Give the extent of all Plasmodium vivax-infected red blood cells.
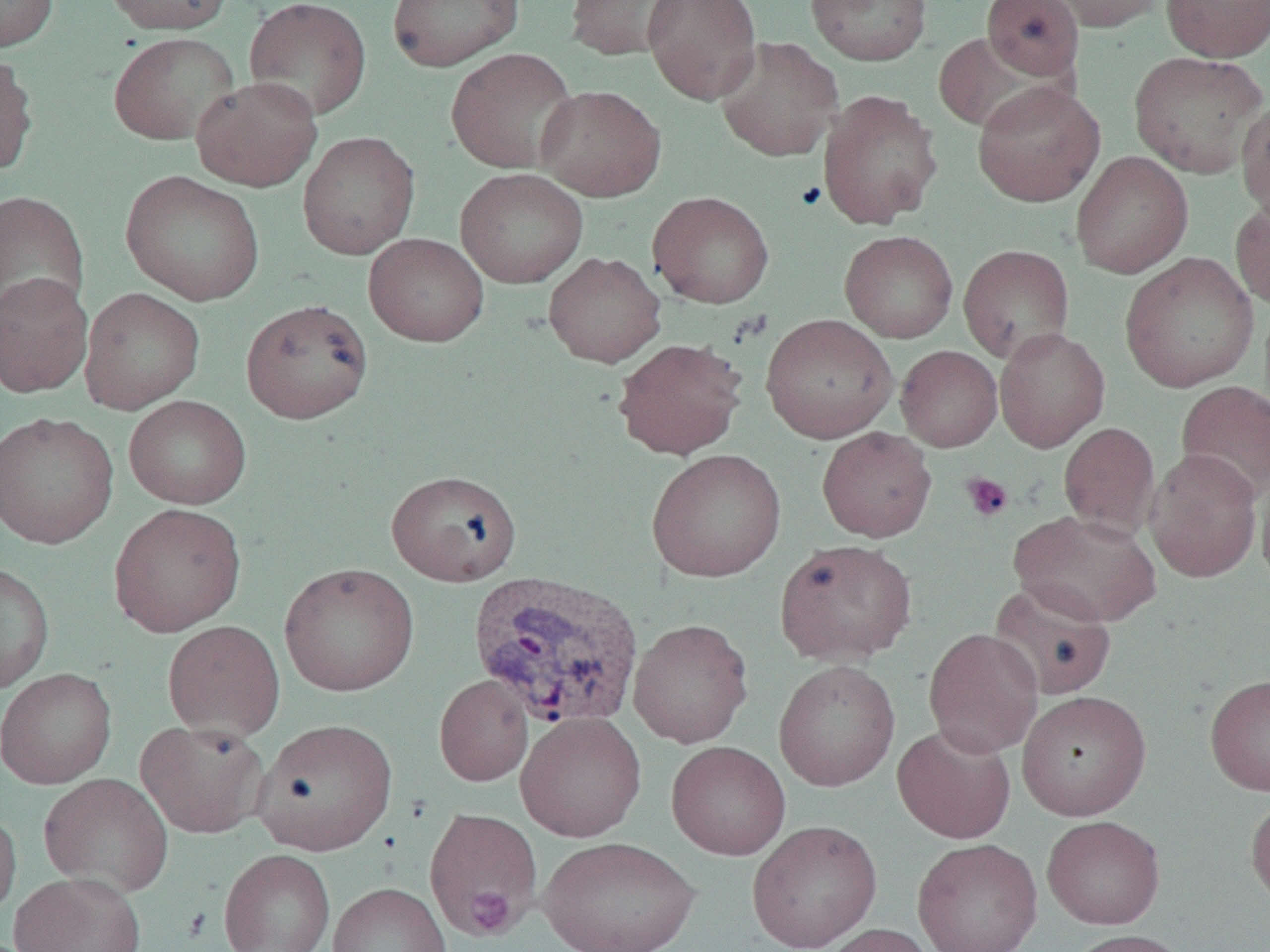

Approximate bounding boxes as [x1, y1, x2, y2] in pixels.
Plasmodium vivax-infected red blood cells: [468, 569, 645, 730].

Platelet locations: [960, 472, 1014, 522], [464, 886, 516, 937]. Uninfected red blood cell locations: [0, 0, 59, 53], [101, 0, 235, 35], [243, 0, 372, 121], [386, 0, 525, 72], [565, 0, 686, 61], [642, 0, 763, 104], [805, 0, 932, 66], [980, 0, 1084, 82], [1040, 0, 1169, 33], [1160, 0, 1270, 62], [933, 30, 1062, 134], [108, 31, 240, 146], [715, 36, 843, 162], [445, 47, 579, 174], [0, 49, 39, 177], [1127, 50, 1268, 178], [192, 75, 322, 191], [971, 80, 1105, 207], [534, 85, 666, 202], [817, 90, 943, 230], [1236, 97, 1270, 224], [298, 131, 420, 260], [1071, 151, 1193, 278], [455, 168, 589, 289], [121, 171, 265, 306], [0, 189, 89, 324], [648, 191, 774, 308], [1230, 196, 1270, 310], [839, 230, 958, 343], [363, 233, 489, 346], [958, 244, 1075, 363], [543, 251, 666, 367], [1119, 252, 1258, 392], [0, 272, 94, 398], [79, 287, 205, 414], [241, 299, 373, 423], [760, 313, 898, 443], [994, 327, 1110, 452], [612, 337, 749, 460], [895, 345, 1002, 452], [1176, 380, 1270, 503], [123, 395, 252, 509], [0, 411, 119, 549], [1058, 422, 1160, 539], [816, 427, 937, 543], [646, 448, 787, 582], [1145, 448, 1263, 583], [1257, 468, 1270, 590], [385, 469, 522, 586], [108, 502, 247, 636], [1010, 509, 1162, 627], [774, 539, 917, 666], [0, 562, 54, 694], [279, 562, 419, 696], [987, 579, 1117, 700], [628, 618, 753, 748], [163, 619, 285, 740], [923, 628, 1044, 757], [773, 659, 900, 791], [0, 667, 117, 789], [1205, 673, 1270, 795], [434, 675, 534, 786], [1016, 690, 1151, 820], [515, 711, 646, 843], [252, 718, 398, 856], [134, 720, 271, 839], [892, 723, 1016, 843], [666, 741, 791, 860], [39, 772, 173, 896], [1246, 793, 1270, 909], [0, 805, 21, 924], [424, 808, 544, 936], [1041, 815, 1165, 929], [746, 819, 882, 952], [538, 835, 701, 952], [912, 837, 1043, 952], [218, 849, 335, 952], [9, 871, 146, 952], [327, 882, 452, 952], [815, 922, 939, 952], [1064, 929, 1196, 952]. Slide-level diagnosis: Plasmodium vivax. Thin blood film. 1000x magnification. Light microscopy. Single field of view. Image is 1270×952 pixels.